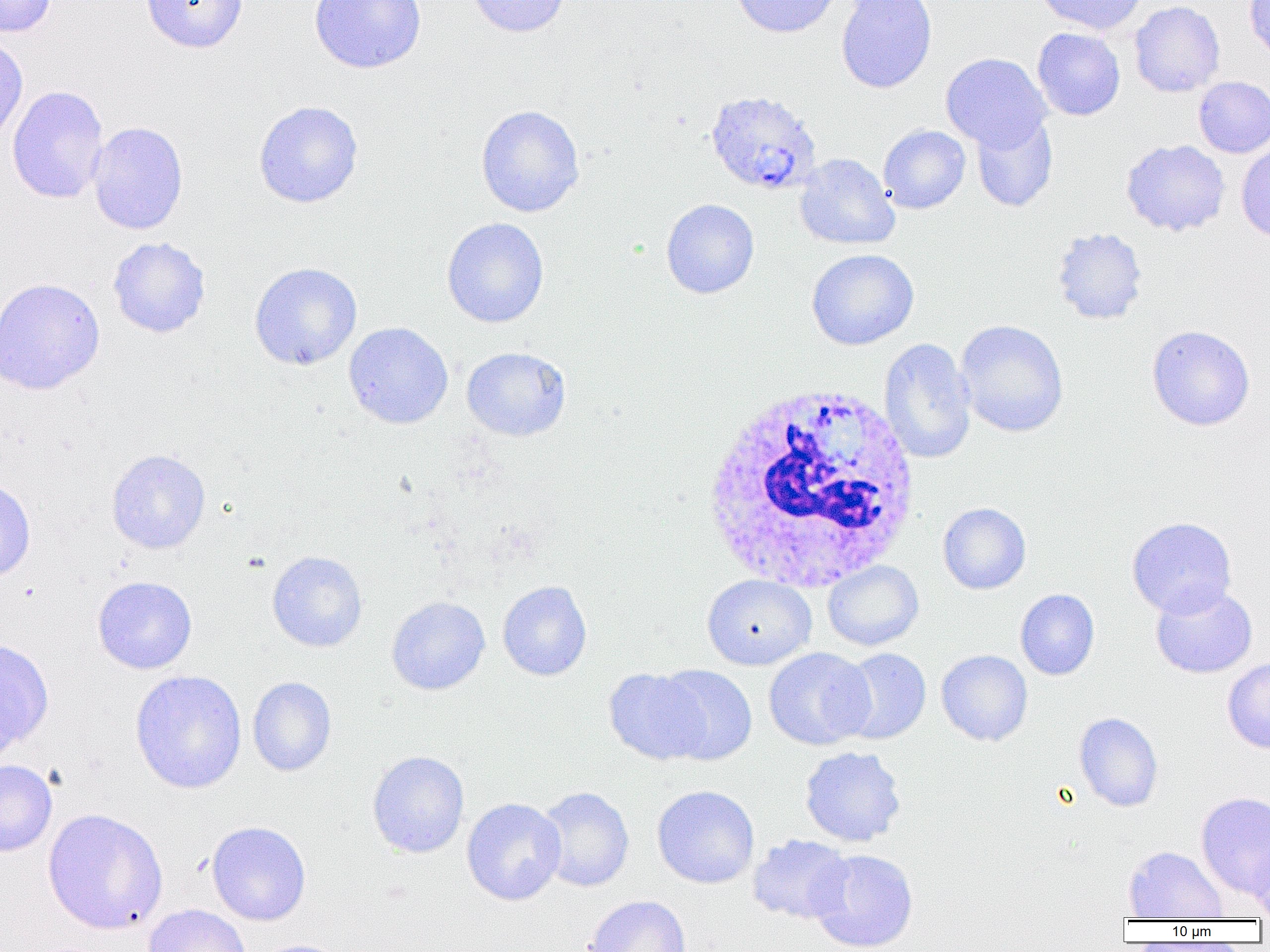
Summary:
  - Coordinate format: approximate bounding boxes as (x1,y1)-(x2,y2) corner pairs in pixels
  - Uninfected red blood cell locations: (0,0)-(57,37), (141,0)-(248,53), (309,0)-(427,74), (465,0)-(572,38), (729,0)-(841,38), (836,0)-(937,93), (1035,0)-(1148,35), (1245,0)-(1270,62), (1129,1)-(1225,98), (1032,28)-(1125,121), (0,34)-(28,146), (940,52)-(1051,151), (1193,76)-(1270,158), (7,85)-(109,205), (253,100)-(364,208), (475,104)-(585,217), (971,113)-(1058,212), (87,121)-(188,235), (878,125)-(971,214), (1120,139)-(1230,237), (1236,141)-(1270,244), (794,152)-(900,250), (660,198)-(760,299), (442,217)-(549,328), (1051,227)-(1148,325), (108,237)-(211,338), (806,249)-(919,350), (249,262)-(362,371), (0,277)-(105,395), (955,319)-(1069,438), (343,322)-(454,429), (1146,325)-(1255,431), (878,337)-(977,464), (461,346)-(571,442), (106,448)-(211,554), (0,478)-(36,583), (938,502)-(1031,594), (1127,516)-(1237,618), (266,550)-(368,653), (822,560)-(924,651), (702,574)-(817,670), (92,575)-(197,674), (497,581)-(592,681), (1150,583)-(1258,678), (1015,589)-(1100,681), (386,596)-(490,695), (0,638)-(54,753), (763,647)-(875,750), (836,648)-(932,745), (936,650)-(1033,746), (1222,657)-(1270,754), (654,665)-(758,765), (603,667)-(712,765), (130,669)-(247,794), (247,676)-(336,777), (1074,712)-(1164,812), (799,746)-(907,847), (367,750)-(470,858), (0,759)-(57,857), (651,785)-(760,889), (535,787)-(635,892), (1195,791)-(1270,899), (462,797)-(566,906), (42,808)-(168,935), (206,821)-(311,926), (747,834)-(854,924), (1248,838)-(1270,920), (1123,845)-(1229,920), (808,849)-(918,951), (584,895)-(691,952), (143,904)-(252,952), (251,939)-(349,952)
  - Plasmodium ovale-infected red blood cell locations: (704,89)-(822,195)
  - White blood cell locations: (698,383)-(922,594)
  - Slide-level diagnosis: Plasmodium ovale
  - Magnification: 1000x
  - Modality: light microscopy
  - Field of view: single
  - Image size: 1270×952 pixels
  - Preparation: thin blood smear